Report the malaria status of this cell.
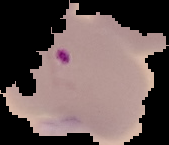
It is parasitized.

Summary:
  - Image size: 169×145 pixels
  - Preparation: thin blood film
  - Image type: cell region segmented out of the field of view; surrounding area masked to black